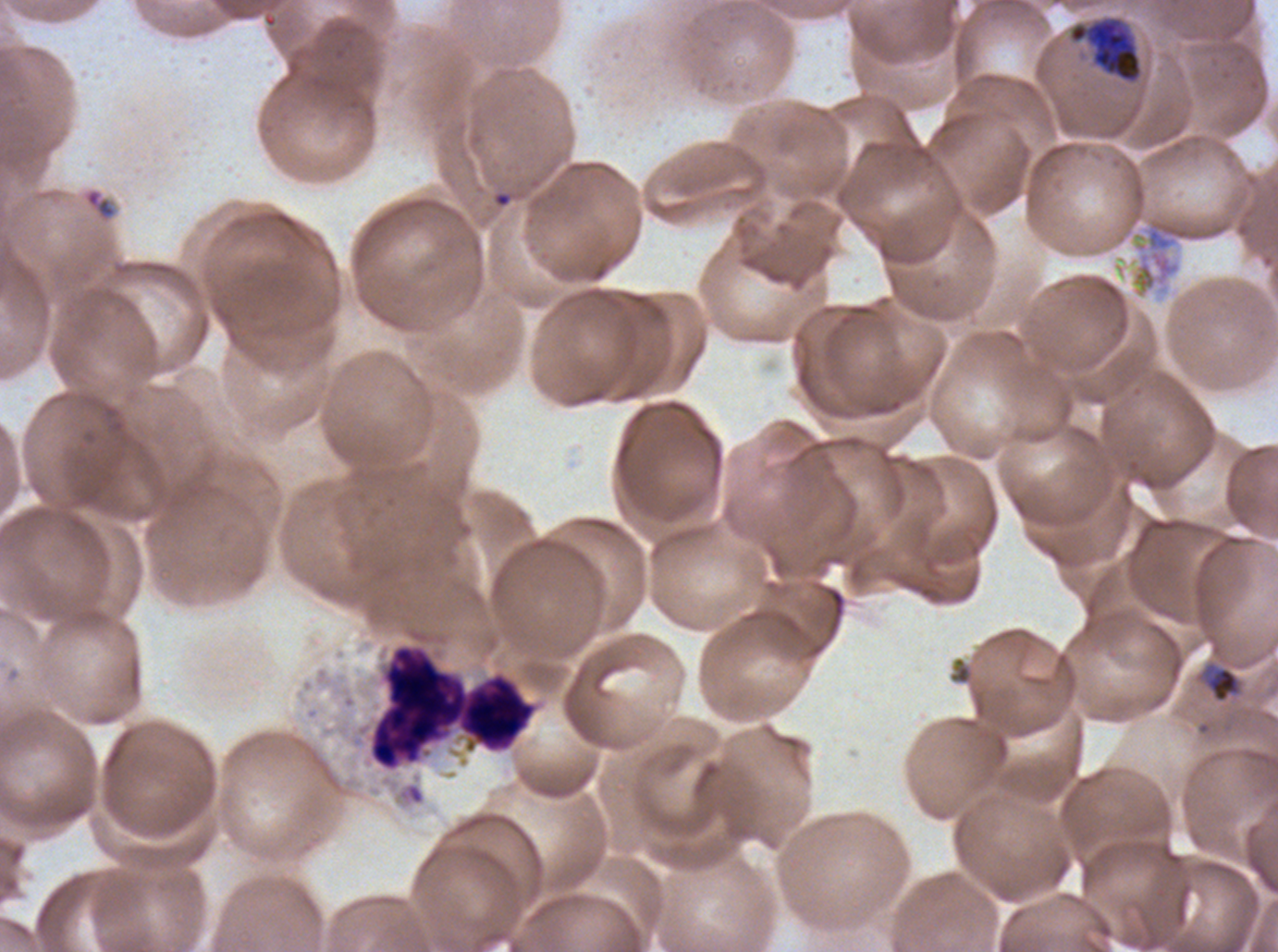 Approximate bounding boxes as (x1, y1, x2, y2) in pixels. Late-ring/early-trophozoite locations: (1204, 664, 1242, 703). Debris locations: (1147, 220, 1206, 250). Late trophozoite locations: (1068, 18, 1142, 82). Leukocyte locations: (369, 645, 536, 770). Life-cycle stages observed: late-ring/early-trophozoite, late trophozoite. Giemsa-stained preparation. A sub-image separated from a larger composite. Image is 1278×952 pixels. Thin blood film. Plasmodium falciparum cultured ex vivo for 24 to 48 hours, from a patient in The Gambia.